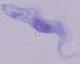

Summary:
  - Magnification: 1000x
  - Identification: trypanosome
  - Modality: micrograph